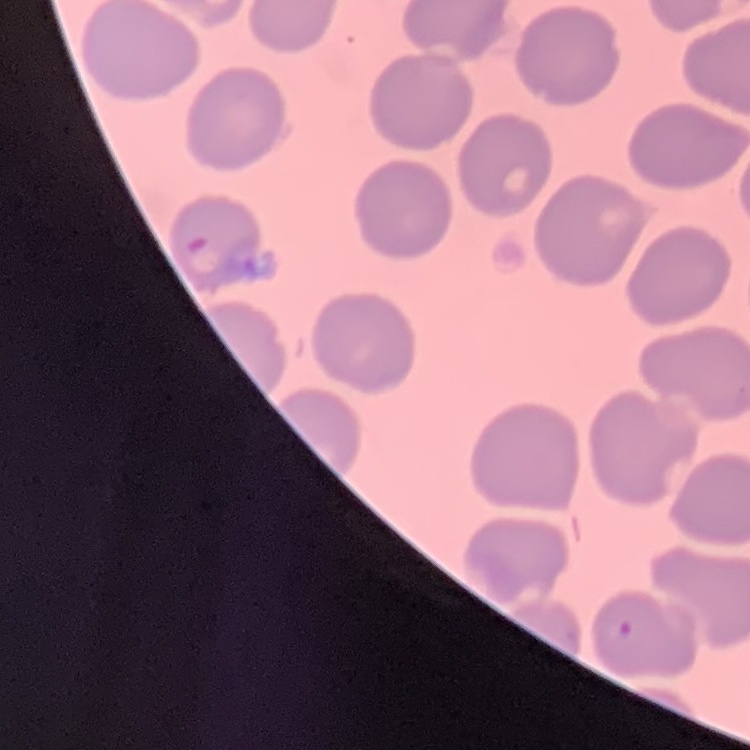

erythrocyte_morphology: no rouleaux formation
image_type: one tile cut from a larger photomicrograph
preparation: thin peripheral smear
stain: Field's or Giemsa